Assess this cell for malaria.
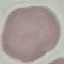

Uninfected.

capture: smartphone camera at the microscope eyepiece
image_type: cell patch, automatically extracted from a larger field of view and resized to 64 × 64 pixels
stain: Giemsa
preparation: thin smear